Assess the morphology of the erythrocytes.
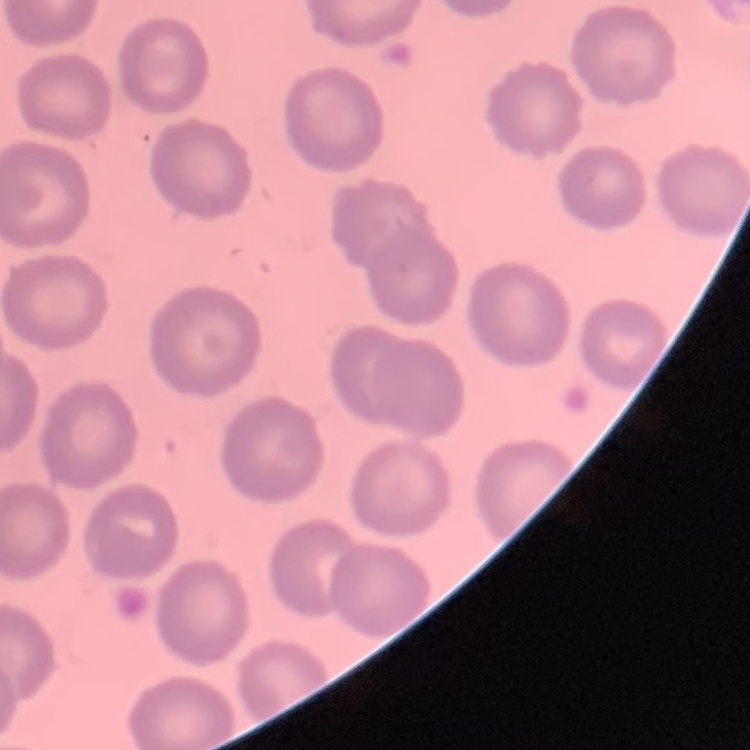

No rouleaux formation.

Summary:
  - Stain: Field's or Giemsa
  - Image type: square crop of a larger photomicrograph
  - Preparation: thin peripheral smear